Name the parasite shown.
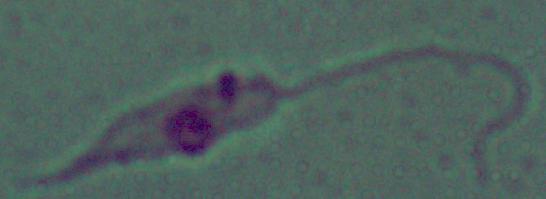
Leishmania.

magnification: 1000x
modality: micrograph